Give the preparation type.
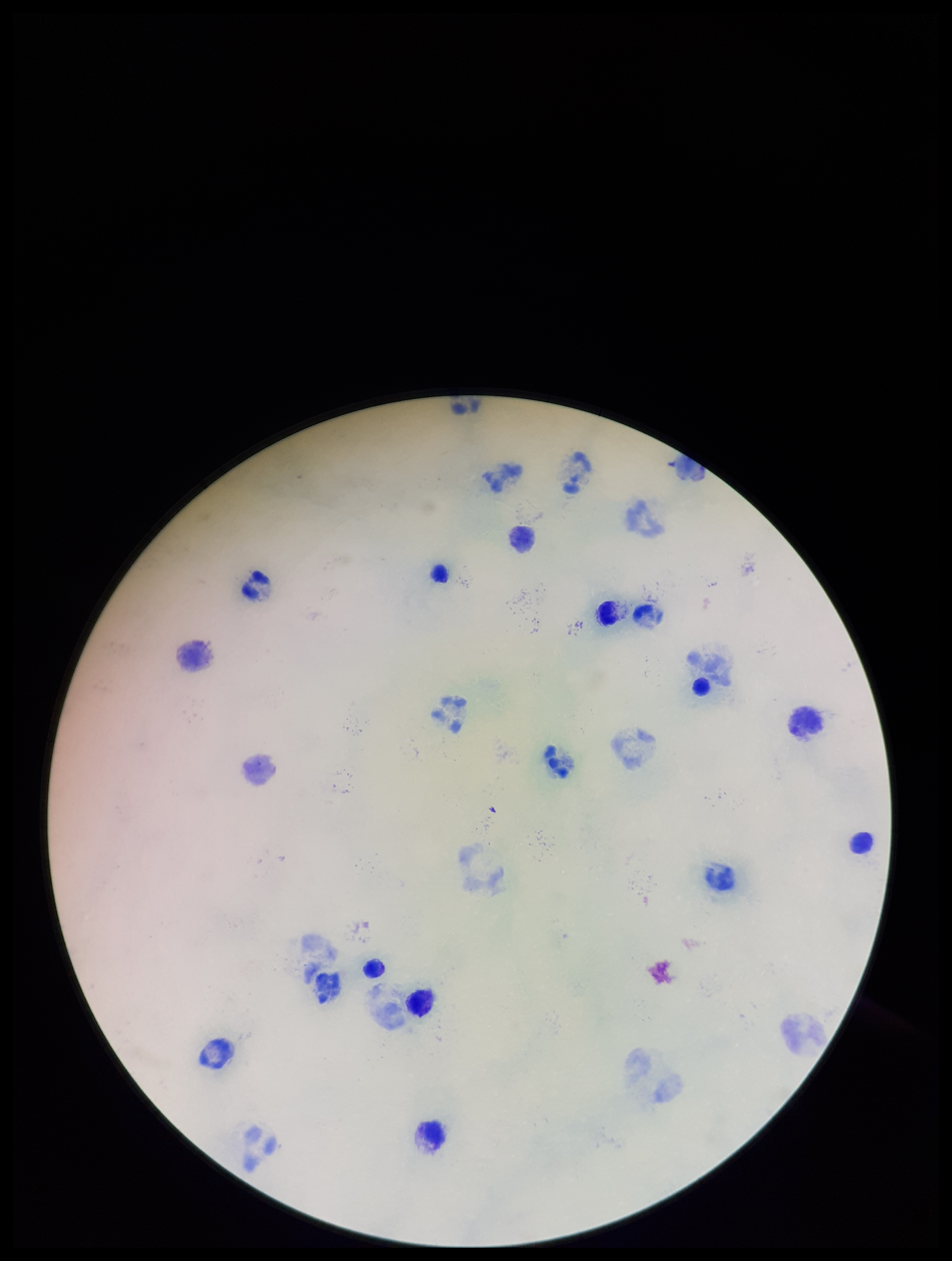

A thick smear.

Leukocyte count: 27. Smartphone photograph taken through the eyepiece of a microscope. Single field of view. Stained with Giemsa. Parasite count: 0. Patient malaria status: negative. Image is 952×1261 pixels. Plasmodium parasites: none seen.